Locate and identify every blood parasite.
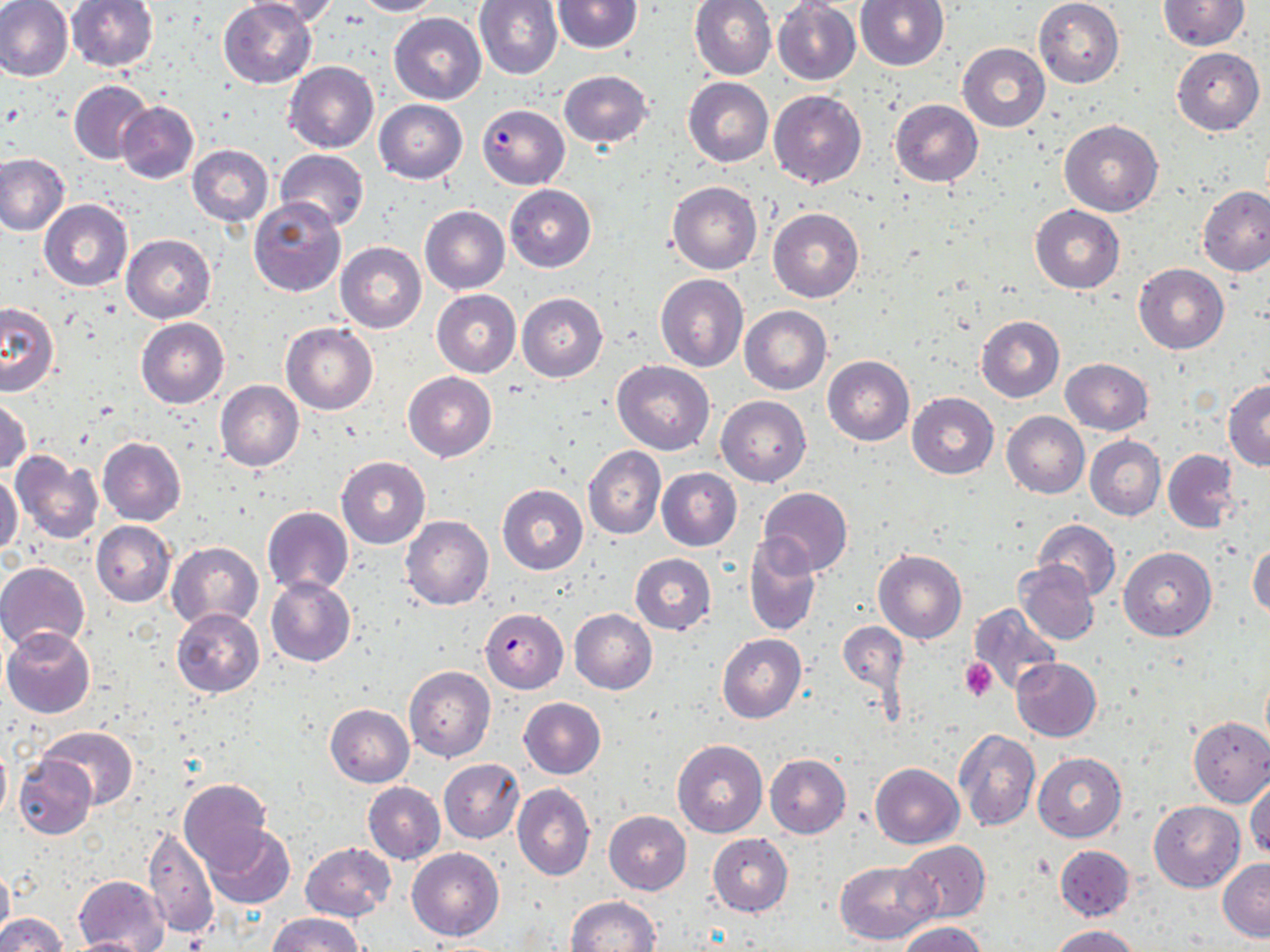

Approximate bounding boxes as [x1, y1, x2, y2] in pixels.
Plasmodium falciparum-infected red blood cells: [476, 110, 578, 188], [480, 608, 569, 693].
No Plasmodium ovale, Plasmodium malariae, Plasmodium vivax, Babesia divergens, or Trypanosoma brucei observed.

Summary:
  - Uninfected red blood cell locations: [66, 0, 160, 72], [244, 0, 345, 28], [354, 0, 445, 17], [1033, 0, 1124, 87], [0, 1, 74, 85], [218, 1, 316, 88], [474, 1, 563, 80], [552, 1, 642, 53], [690, 1, 777, 79], [853, 1, 949, 71], [1158, 1, 1248, 51], [773, 2, 860, 85], [388, 12, 486, 103], [958, 42, 1051, 132], [1171, 47, 1264, 134], [283, 62, 379, 153], [558, 70, 653, 150], [683, 77, 773, 167], [69, 80, 155, 166], [768, 90, 867, 189], [374, 99, 467, 183], [890, 99, 983, 186], [115, 100, 199, 184], [1059, 121, 1163, 217], [187, 145, 274, 226], [275, 149, 369, 232], [0, 154, 71, 237], [667, 181, 762, 274], [505, 185, 596, 271], [1197, 186, 1269, 276], [249, 196, 345, 297], [38, 199, 132, 292], [420, 204, 510, 295], [1030, 205, 1124, 293], [768, 208, 864, 304], [122, 234, 215, 323], [335, 242, 426, 333], [1134, 264, 1229, 353], [656, 273, 748, 372], [432, 290, 521, 376], [517, 293, 607, 382], [0, 301, 59, 396], [741, 305, 832, 394], [976, 316, 1064, 403], [136, 317, 229, 408], [281, 324, 378, 414], [823, 356, 914, 446], [1061, 357, 1152, 434], [611, 361, 714, 455], [404, 372, 495, 462], [215, 380, 303, 471], [1225, 381, 1270, 470], [907, 392, 999, 478], [1, 396, 32, 476], [717, 396, 811, 486], [1001, 412, 1089, 498], [1085, 435, 1164, 520], [97, 436, 186, 526], [586, 447, 668, 541], [1163, 449, 1240, 533], [11, 452, 104, 544], [337, 457, 430, 548], [657, 468, 741, 551], [0, 471, 22, 555], [497, 485, 588, 574], [757, 487, 852, 577], [262, 506, 353, 596], [401, 516, 494, 610], [1032, 518, 1120, 601], [91, 520, 175, 606], [743, 538, 821, 637], [1247, 539, 1269, 620], [167, 542, 263, 630], [1119, 546, 1216, 641], [874, 550, 967, 644], [629, 553, 716, 635], [0, 560, 89, 653], [1014, 560, 1100, 645], [266, 577, 356, 667], [969, 604, 1060, 698], [172, 609, 264, 697], [570, 609, 656, 694], [837, 620, 908, 707], [1, 627, 97, 716], [717, 633, 806, 723], [1012, 658, 1101, 742], [404, 666, 495, 761], [518, 697, 606, 779], [325, 704, 414, 786], [1188, 716, 1270, 806], [38, 726, 140, 809], [955, 731, 1041, 832], [672, 740, 767, 837], [0, 741, 11, 824], [1034, 753, 1126, 842], [765, 754, 850, 837], [13, 756, 96, 839], [439, 759, 524, 843], [870, 763, 963, 848], [1246, 777, 1270, 861], [179, 779, 272, 870], [362, 781, 445, 864], [512, 783, 594, 880], [1149, 801, 1244, 891], [603, 812, 691, 894], [143, 824, 217, 938], [202, 824, 295, 909], [707, 833, 793, 916], [898, 840, 991, 923], [300, 842, 396, 922], [1056, 845, 1134, 921], [407, 847, 504, 941], [1218, 858, 1270, 942], [835, 860, 937, 945], [0, 861, 13, 947], [75, 876, 168, 950], [566, 896, 661, 952], [0, 912, 65, 952], [266, 912, 364, 952], [898, 922, 989, 952], [1048, 925, 1140, 952], [63, 936, 157, 951]
  - Platelet locations: [960, 657, 998, 701]
  - Slide-level diagnosis: Plasmodium falciparum
  - Preparation: thin blood film
  - Image size: 1270×952 pixels
  - Modality: optical microscopy
  - Magnification: 1000x
  - Stain: May-Grünwald-Giemsa
  - Field of view: single